Comment on the morphology of the erythrocytes.
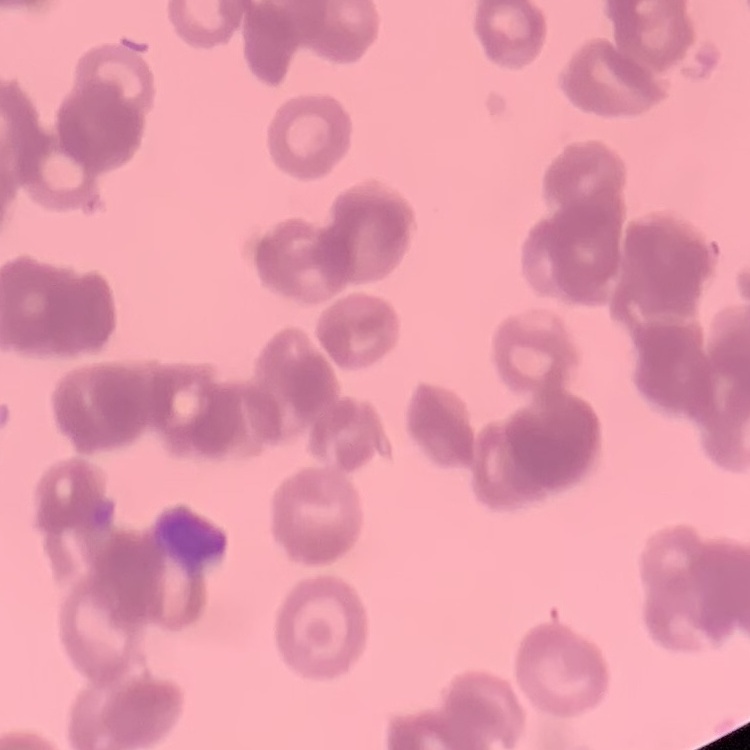
Rouleaux formation.

Summary:
  - Stain: Field's or Giemsa
  - Image type: square crop of a larger photomicrograph
  - Preparation: thin blood film